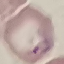

Summary:
  - Malaria status: parasitized
  - Preparation: thin smear
  - Capture: smartphone through the microscope eyepiece
  - Image type: cell patch, automatically extracted from a larger field of view and resized to 64 × 64 pixels
  - Stain: Giemsa